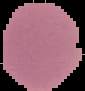

image_size: 85×91 pixels
preparation: thin blood smear
result: no Plasmodium parasites detected
image_type: cell region segmented out of the field of view; surrounding area masked to black